Locate every Plasmodium parasite.
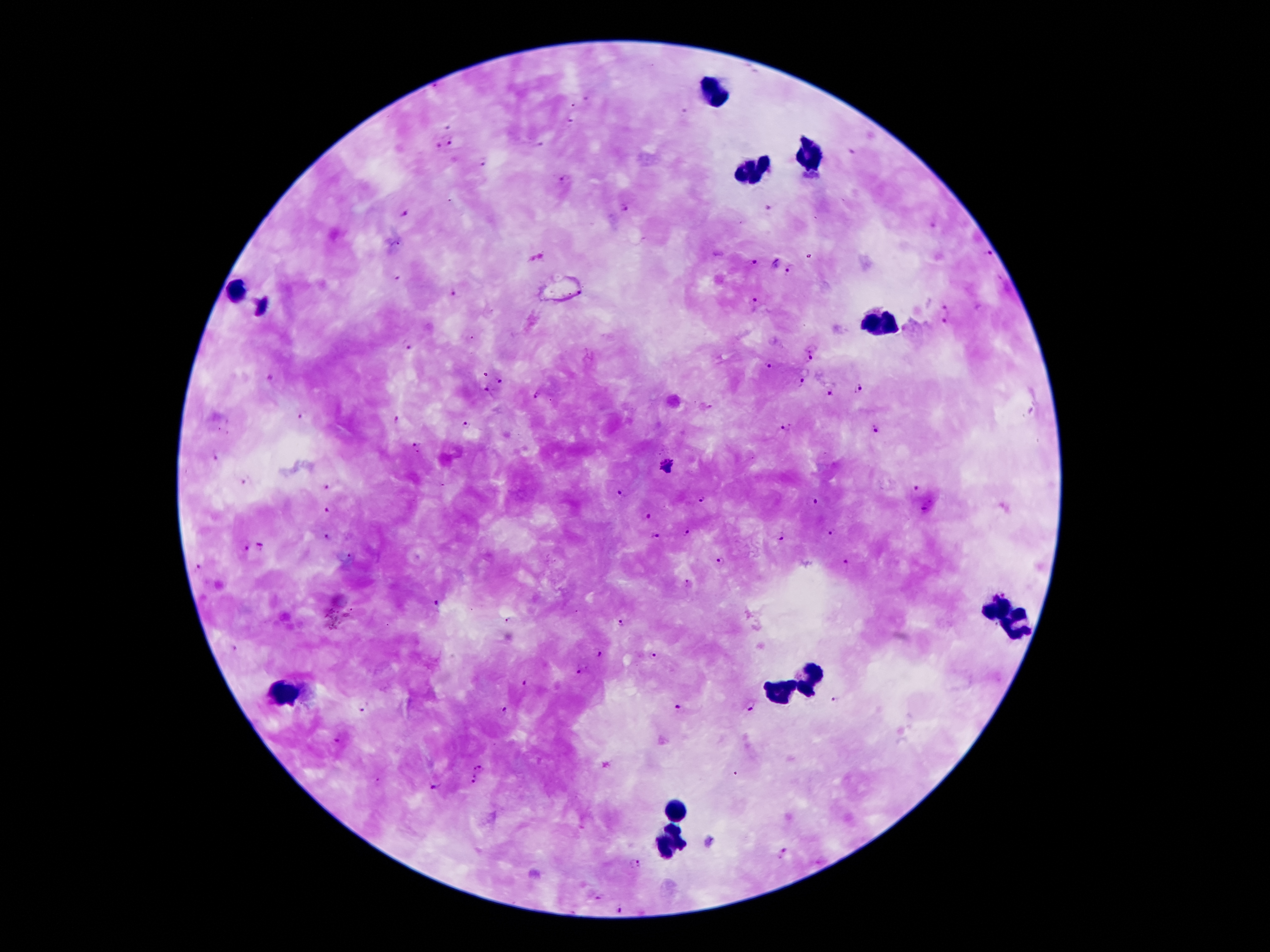
Approximate centers as (x, y) in pixels.
Plasmodium parasites: (685, 112), (570, 121), (450, 144), (538, 145), (438, 146), (852, 153), (484, 160), (562, 179), (625, 208), (404, 213), (989, 253), (536, 258), (751, 264), (791, 270), (397, 279), (452, 293), (756, 305), (944, 308), (944, 321), (406, 347), (811, 357), (770, 366), (500, 380), (801, 381), (858, 388), (487, 390), (829, 394), (537, 396), (303, 417), (396, 421), (467, 423), (786, 426), (875, 429), (414, 447), (215, 457), (667, 465), (243, 482), (325, 487), (918, 489), (622, 493), (701, 498), (816, 503), (326, 509), (924, 509), (647, 515), (828, 532), (687, 533), (780, 535), (327, 537), (656, 538), (260, 545), (245, 549), (720, 561), (845, 562), (202, 567), (684, 581), (436, 605), (508, 621), (621, 624), (236, 647), (599, 652), (655, 655), (579, 671), (526, 685), (837, 700), (750, 705), (362, 708), (680, 708), (503, 711), (336, 740), (478, 769), (475, 780), (435, 784), (783, 852), (635, 864), (600, 896), (621, 910).

Summary:
  - Leukocyte locations: (714, 94), (809, 156), (751, 170), (238, 290), (888, 325), (998, 607), (1019, 626), (809, 677), (783, 691), (287, 693), (676, 812), (672, 843)
  - Image size: 1270×952 pixels
  - Capture: smartphone camera through the microscope eyepiece
  - Patient malaria status: infected with Plasmodium falciparum
  - Stain: Giemsa
  - Magnification: 100x
  - Field of view: single
  - Preparation: thick blood smear